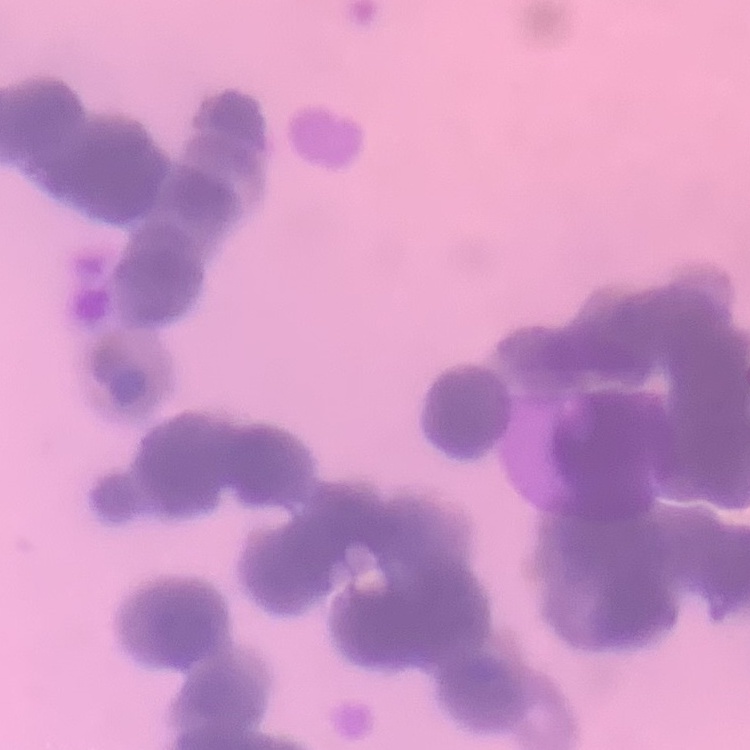

The erythrocytes show rouleaux formation. One tile cut from a larger photomicrograph. Field's or Giemsa stain. Thin blood smear.